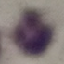 Malaria status: uninfected. Acquired by smartphone through the microscope eyepiece. Thin blood smear. Automatically extracted cell patch, resized to 64 × 64 pixels. Giemsa stain.